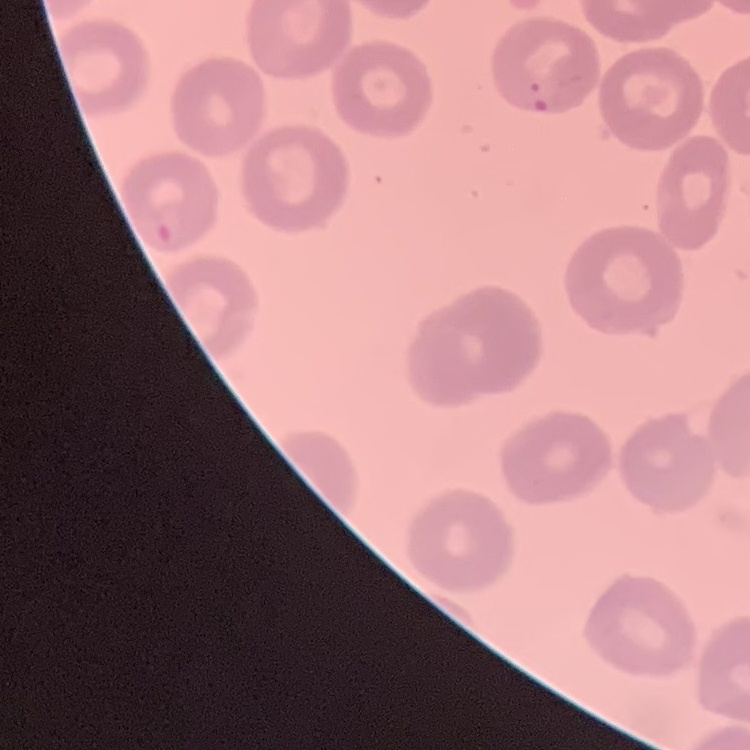
{
  "erythrocyte_morphology": "no rouleaux formation",
  "preparation": "thin blood smear",
  "image_type": "one tile cut from a larger photomicrograph",
  "stain": "Field's or Giemsa"
}